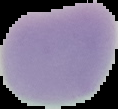
preparation: thin blood film
image_size: 118×109 pixels
malaria_status: uninfected
image_type: cell region segmented out of the field of view; surrounding area masked to black